Identify the cell.
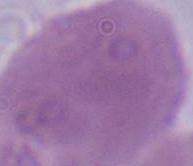
An erythrocyte.

Summary:
  - Magnification: 1000x
  - Modality: micrograph